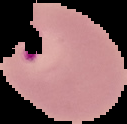
image_type: segmented cell region on a black background
result: Plasmodium parasites identified
image_size: 127×124 pixels
preparation: thin blood smear